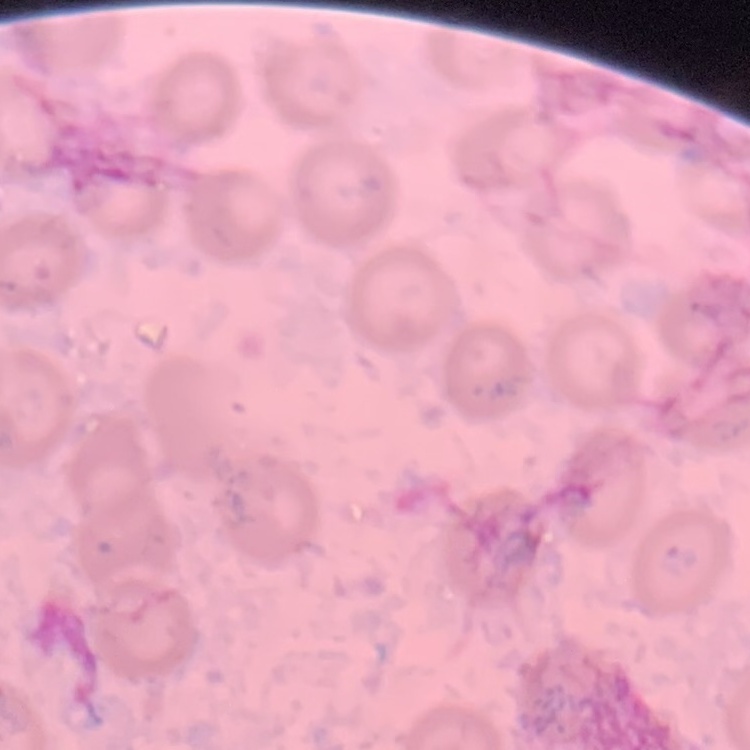 The erythrocytes show no rouleaux formation. Stained with either Field's or Giemsa. Thin blood smear. One tile cut from a larger photomicrograph.